Outline each blood parasite and name the species.
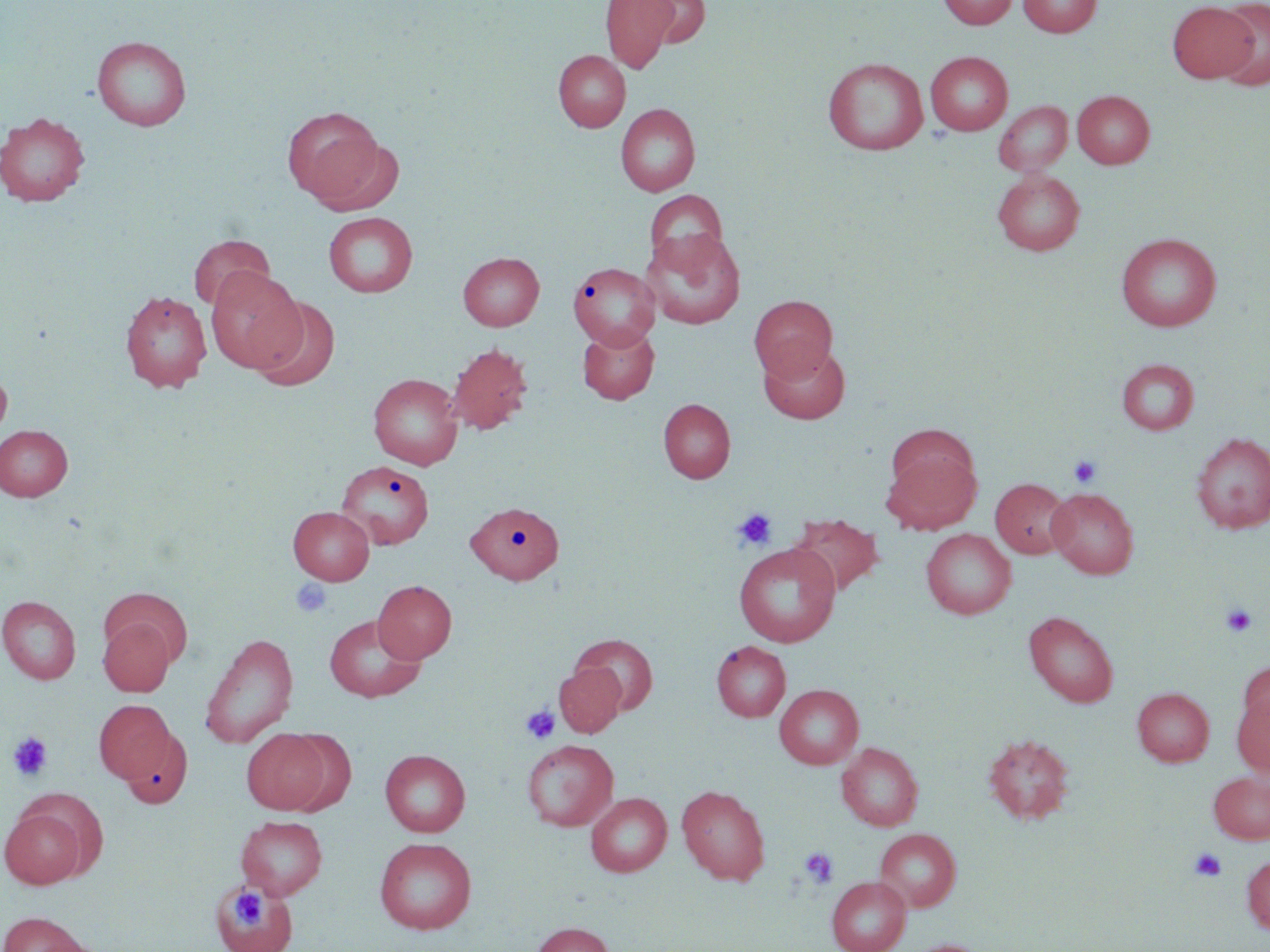
No blood parasites observed.

Approximate bounding boxes as [x1, y1, x2, y2] in pixels. Uninfected red blood cell locations: [600, 0, 677, 74], [637, 0, 711, 49], [937, 0, 1018, 29], [1017, 0, 1102, 38], [1214, 0, 1270, 91], [1167, 1, 1257, 84], [91, 35, 192, 131], [553, 50, 630, 132], [925, 50, 1013, 135], [823, 57, 929, 155], [1072, 90, 1155, 169], [993, 101, 1073, 176], [615, 103, 700, 196], [282, 106, 383, 203], [0, 112, 91, 207], [305, 135, 405, 216], [992, 169, 1085, 256], [644, 189, 728, 270], [323, 212, 418, 297], [642, 229, 746, 330], [1116, 232, 1221, 331], [188, 234, 274, 313], [458, 252, 544, 330], [568, 261, 660, 349], [205, 267, 305, 372], [120, 290, 212, 393], [749, 295, 837, 382], [251, 297, 341, 392], [578, 325, 660, 404], [758, 342, 851, 424], [446, 343, 533, 435], [1117, 358, 1200, 435], [0, 366, 12, 443], [369, 373, 463, 469], [659, 398, 735, 483], [0, 425, 72, 501], [1191, 432, 1270, 533], [883, 449, 980, 535], [336, 459, 434, 549], [990, 478, 1073, 559], [1047, 488, 1139, 578], [464, 502, 572, 587], [289, 506, 374, 585], [789, 514, 885, 597], [921, 529, 1016, 619], [734, 542, 841, 647], [373, 580, 456, 663], [102, 589, 193, 668], [0, 596, 81, 684], [1023, 611, 1118, 707], [324, 614, 426, 703], [99, 618, 175, 696], [199, 632, 298, 748], [570, 634, 659, 715], [712, 642, 791, 722], [1239, 662, 1270, 737], [554, 663, 625, 737], [775, 684, 864, 769], [1132, 687, 1214, 766], [1232, 693, 1270, 777], [94, 700, 177, 785], [242, 729, 331, 814], [127, 732, 192, 810], [984, 733, 1075, 824], [522, 739, 618, 831], [837, 742, 923, 831], [380, 749, 470, 837], [1208, 771, 1270, 844], [677, 785, 770, 884], [586, 792, 671, 877], [1, 806, 89, 888], [236, 815, 327, 899], [874, 828, 961, 912], [374, 837, 476, 934], [1242, 854, 1270, 935], [827, 877, 911, 952], [214, 883, 296, 952], [0, 912, 90, 952], [533, 922, 614, 952], [902, 939, 989, 952]. Platelet locations: [1069, 456, 1102, 488], [733, 509, 776, 550], [290, 579, 333, 618], [1220, 602, 1257, 636], [520, 705, 560, 745], [8, 732, 54, 782], [1189, 847, 1226, 882], [800, 848, 838, 887], [231, 888, 265, 926]. Slide-level diagnosis: negative for blood parasites. One field of a larger specimen. Thin blood smear. May-Grünwald-Giemsa-stained preparation. 1000x magnification. Image is 1270×952 pixels. Light microscopy.